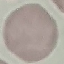

result: no malaria parasites seen
stain: Giemsa
image_type: cell patch, automatically extracted from a larger field of view and resized to 64 × 64 pixels
preparation: thin blood smear
capture: smartphone camera at the microscope eyepiece